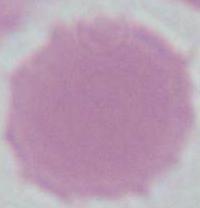
Summary:
  - Magnification: 1000x
  - Modality: micrograph
  - Identification: erythrocyte